Give the extent of all Plasmodium falciparum-infected red blood cells.
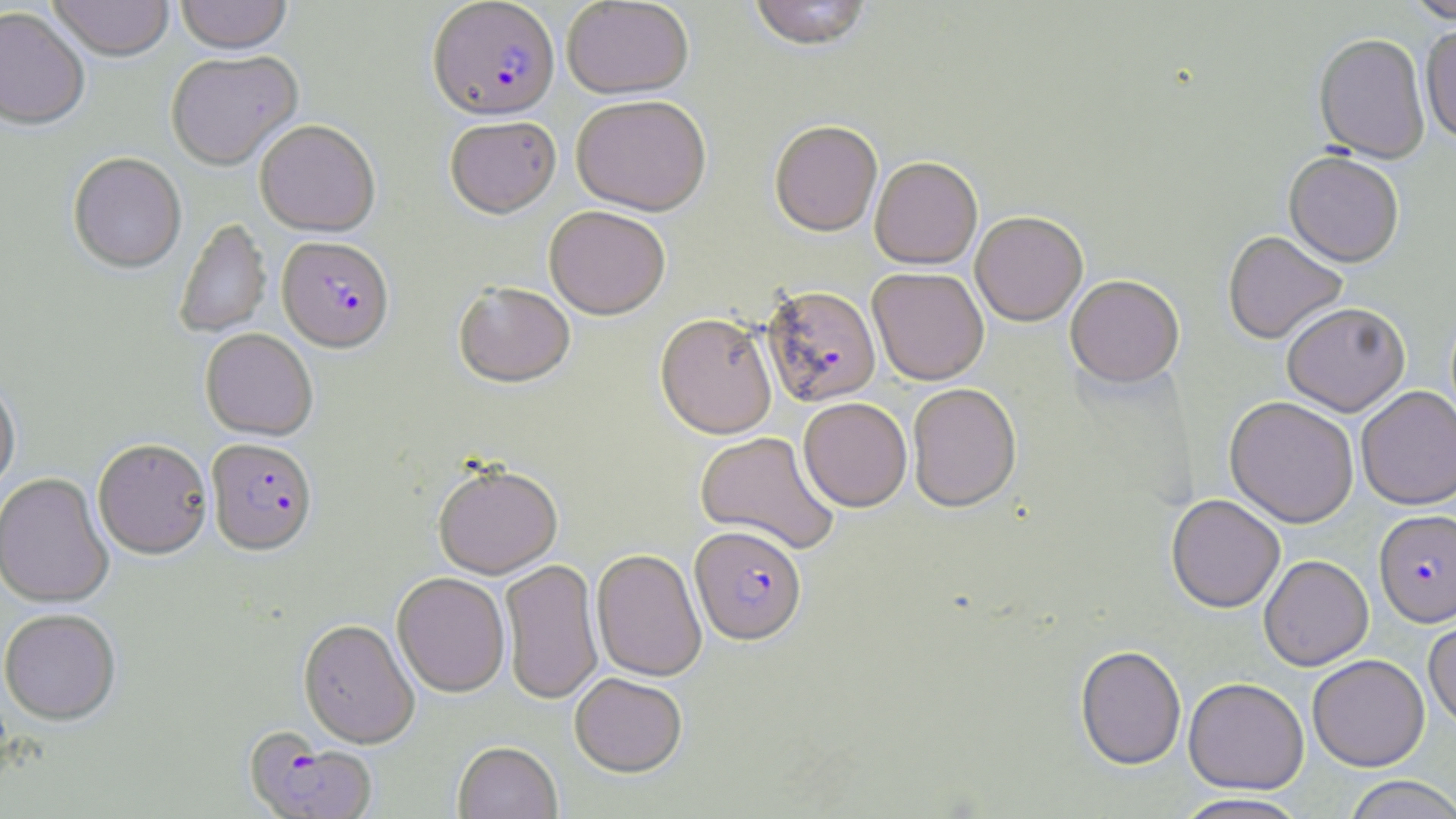
Approximate bounding boxes as (x1,y1)-(x2,y2) corner pairs in pixels.
Plasmodium falciparum-infected red blood cells: (427,1)-(560,124), (277,239)-(395,355), (762,286)-(881,408), (206,440)-(318,558), (1375,509)-(1456,627), (690,528)-(806,647), (243,729)-(378,819).

{
  "slide_level_diagnosis": "Plasmodium falciparum",
  "uninfected_red_blood_cell_locations": "approximate bounding boxes as (x1,y1)-(x2,y2) corner pairs in pixels: (47,0)-(175,64), (175,0)-(292,57), (562,0)-(694,100), (747,0)-(873,53), (1403,0)-(1456,24), (0,8)-(89,133), (1420,27)-(1456,145), (1313,34)-(1431,164), (165,53)-(304,172), (571,97)-(711,219), (445,119)-(561,222), (255,122)-(381,238), (770,123)-(883,237), (1283,152)-(1404,268), (68,154)-(186,275), (870,158)-(982,270), (544,208)-(671,322), (971,213)-(1087,326), (174,219)-(271,338), (1222,231)-(1347,345), (868,268)-(989,385), (1065,276)-(1184,388), (454,284)-(576,390), (1282,302)-(1410,416), (655,315)-(777,440), (200,329)-(317,442), (0,379)-(21,496), (907,383)-(1021,514), (1356,386)-(1456,509), (1225,395)-(1359,527), (798,398)-(912,512), (696,432)-(840,556), (93,440)-(212,561), (433,466)-(563,580), (0,473)-(114,610), (1166,494)-(1285,613), (591,550)-(707,682), (1259,555)-(1373,671), (500,560)-(604,705), (392,574)-(510,698), (0,611)-(121,727), (1423,613)-(1456,731), (298,620)-(420,750), (1075,645)-(1186,769), (1307,653)-(1430,771), (570,674)-(687,779), (1183,677)-(1309,794), (453,743)-(563,819), (1342,775)-(1456,818), (1171,793)-(1312,819)",
  "stain": "May-Grünwald-Giemsa",
  "field_of_view": "single",
  "magnification": "1000x",
  "image_size": "1456×819 pixels",
  "preparation": "thin blood smear",
  "modality": "light microscopy"
}